Comment on the morphology of the red blood cells.
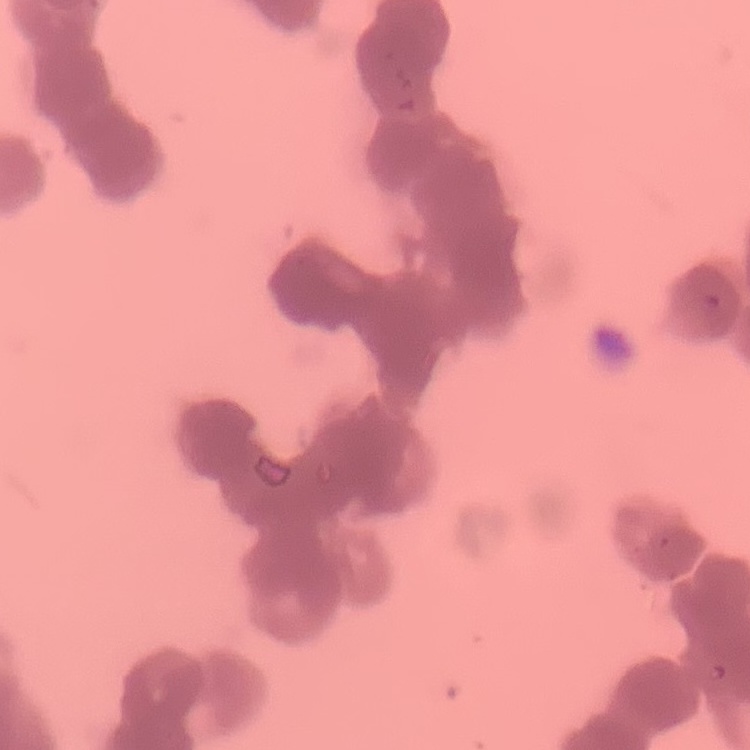
They show rouleaux formation.

Summary:
  - Stain: Field's or Giemsa
  - Image type: square crop of a larger photomicrograph
  - Preparation: thin blood smear